Assess this cell for malaria.
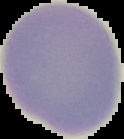

Uninfected.

From a thin blood smear. Segmented cell region on a black background. Image is 124×139 pixels.